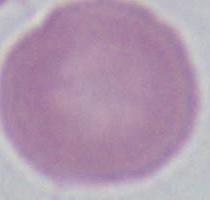

A red blood cell is shown. Captured at 1000x magnification. Photomicrograph.